Identify the blood parasite species.
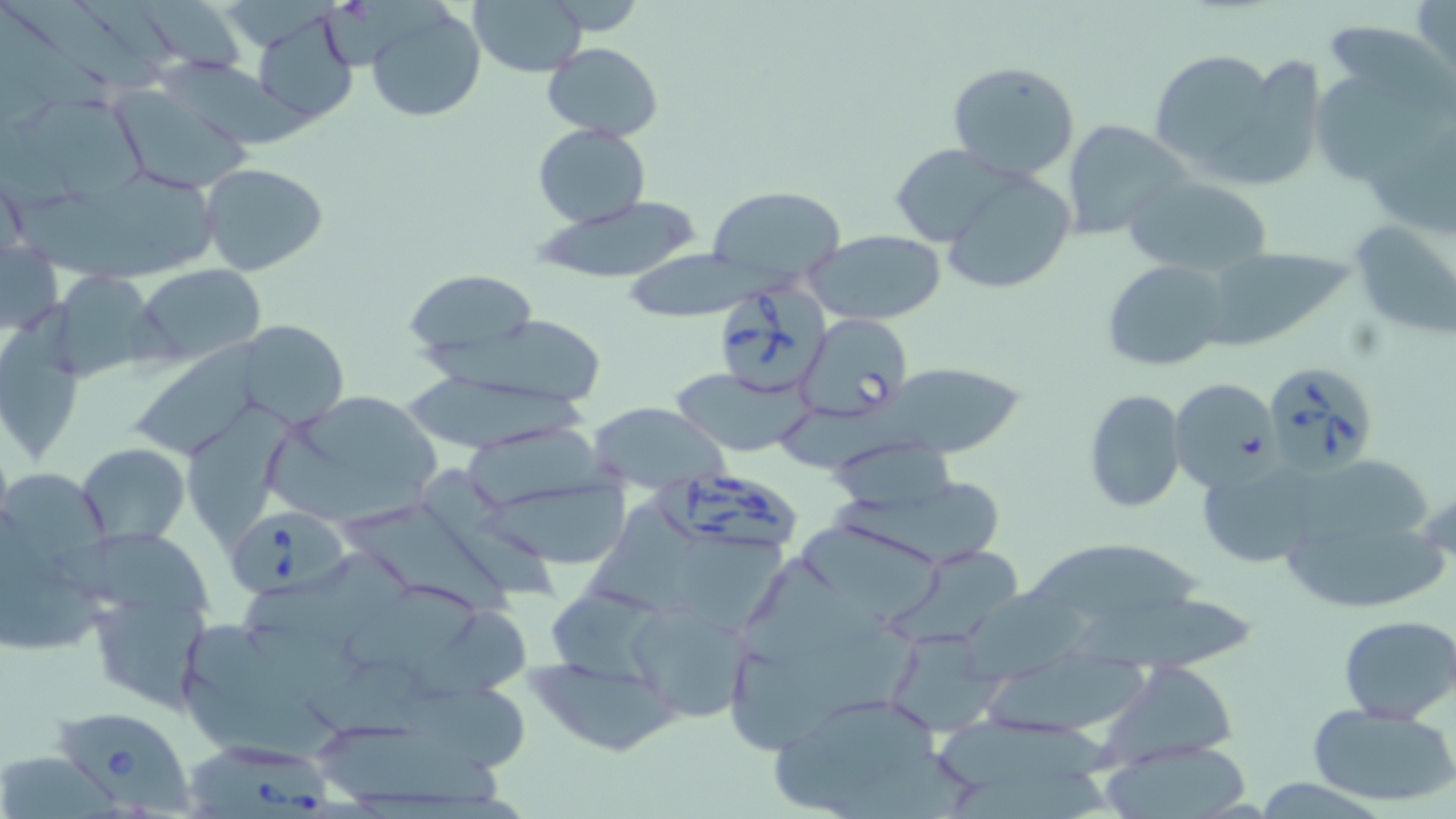

Babesia divergens.

Approximate bounding boxes as (x1, y1, x2, y2) in pixels. Babesia divergens-infected red blood cell locations: (717, 286, 830, 399), (798, 313, 912, 419), (1261, 359, 1380, 476), (644, 470, 796, 550), (229, 509, 355, 602), (52, 707, 194, 811), (180, 732, 332, 817). Uninfected red blood cell locations: (3, 0, 158, 92), (76, 0, 175, 69), (469, 0, 589, 76), (1414, 0, 1456, 86), (141, 1, 245, 73), (0, 4, 109, 108), (366, 4, 487, 122), (251, 11, 360, 125), (1319, 18, 1455, 111), (542, 41, 662, 142), (1149, 48, 1282, 174), (1212, 54, 1324, 186), (153, 56, 317, 150), (1311, 59, 1448, 182), (946, 61, 1081, 181), (109, 85, 254, 194), (30, 98, 153, 203), (1061, 119, 1193, 240), (533, 124, 651, 226), (888, 144, 1021, 247), (199, 162, 328, 275), (937, 167, 1077, 295), (105, 170, 218, 260), (1121, 173, 1275, 277), (706, 184, 847, 290), (12, 194, 187, 284), (530, 195, 708, 286), (1348, 217, 1456, 339), (804, 229, 948, 326), (1, 240, 64, 337), (1202, 248, 1353, 350), (1101, 257, 1230, 372), (136, 265, 265, 364), (403, 269, 542, 365), (59, 270, 180, 382), (0, 296, 94, 462), (239, 321, 347, 426), (138, 342, 261, 458), (881, 363, 1027, 458), (670, 369, 809, 456), (406, 370, 591, 452), (1168, 377, 1281, 490), (1084, 389, 1186, 513), (268, 391, 441, 524), (189, 397, 295, 550), (588, 403, 730, 489), (777, 405, 931, 474), (464, 428, 616, 510), (826, 437, 961, 517), (77, 443, 189, 545), (1307, 457, 1431, 549), (1197, 459, 1321, 569), (416, 468, 557, 608), (2, 470, 111, 576), (479, 479, 634, 573), (825, 480, 1002, 567), (597, 501, 703, 618), (350, 506, 521, 619), (798, 519, 949, 623), (1287, 523, 1446, 611), (56, 530, 213, 618), (677, 534, 787, 635), (1026, 534, 1204, 623), (242, 548, 416, 643), (888, 551, 1018, 644), (743, 557, 921, 705), (0, 570, 108, 652), (349, 585, 483, 673), (549, 588, 661, 686), (962, 590, 1100, 685), (86, 594, 208, 710), (1076, 595, 1257, 678), (629, 600, 756, 724), (408, 609, 529, 699), (1338, 614, 1456, 724), (182, 621, 312, 715), (885, 627, 1005, 737), (985, 651, 1150, 738), (530, 657, 684, 757), (308, 659, 445, 741), (1107, 661, 1241, 766), (184, 670, 340, 768), (405, 685, 531, 779), (770, 694, 956, 815), (1306, 701, 1456, 809), (931, 712, 1117, 783), (321, 724, 506, 806), (1100, 738, 1257, 819), (0, 755, 119, 819), (949, 770, 1110, 819). Light microscopy. Image is 1456×819 pixels. One field of a larger specimen. Captured at 1000x magnification. Thin blood film. May-Grünwald-Giemsa-stained preparation.